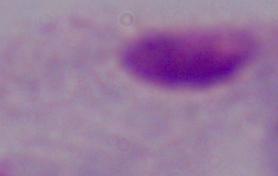
magnification = 1000x
modality = micrograph
identification = trichomonad